Classify this cell by malaria status.
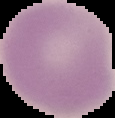
It is uninfected.

preparation = thin blood film
image size = 115×118 pixels
image type = cell region segmented out of the field of view; surrounding area masked to black